Identify the parasite.
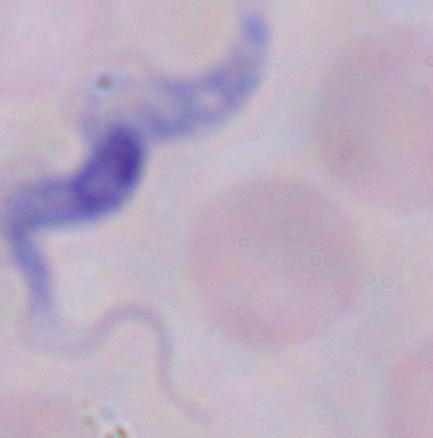
This is a trypanosome.

Photomicrograph. 1000x magnification.